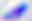 400x magnification. Photomicrograph. Toxoplasma gondii is seen.